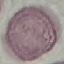
Summary:
  - Result: no malaria parasites seen
  - Capture: smartphone camera at the microscope eyepiece
  - Preparation: thin blood smear
  - Image type: cell patch, automatically extracted from a larger field of view and resized to 64 × 64 pixels
  - Stain: Giemsa